Point out each Plasmodium parasite.
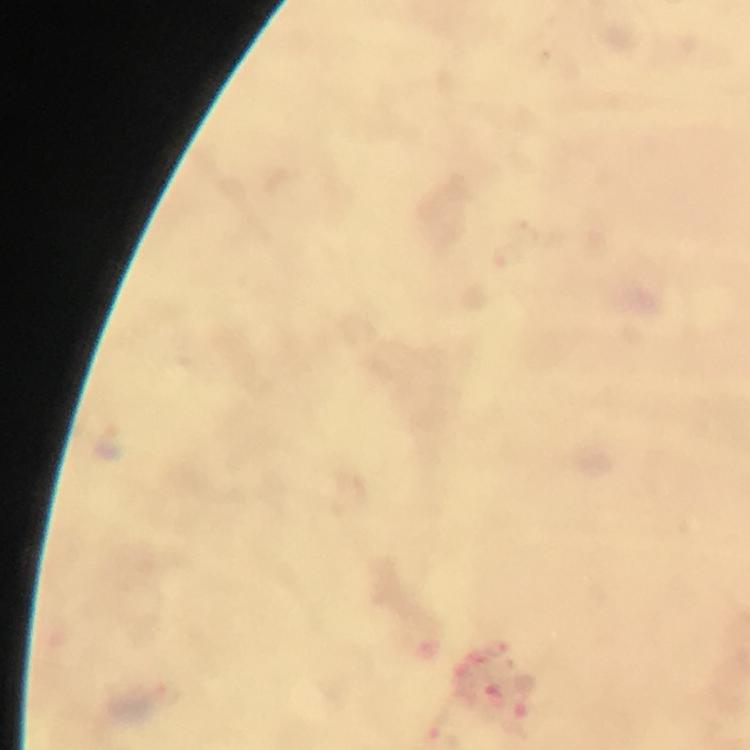
Approximate object centers, in pixels from the top-left corner.
Plasmodium parasites: (x=508, y=258), (x=111, y=440).

Summary:
  - Context: from a diagnostic examination for malaria
  - Preparation: thick blood smear
  - Cropped from: one field of view
  - Stain: Giemsa
  - Image size: 750×750 pixels
  - Immersion oil: applied
  - Capture: smartphone mounted on the microscope
  - Magnification: 100x